Point out each leukocyte.
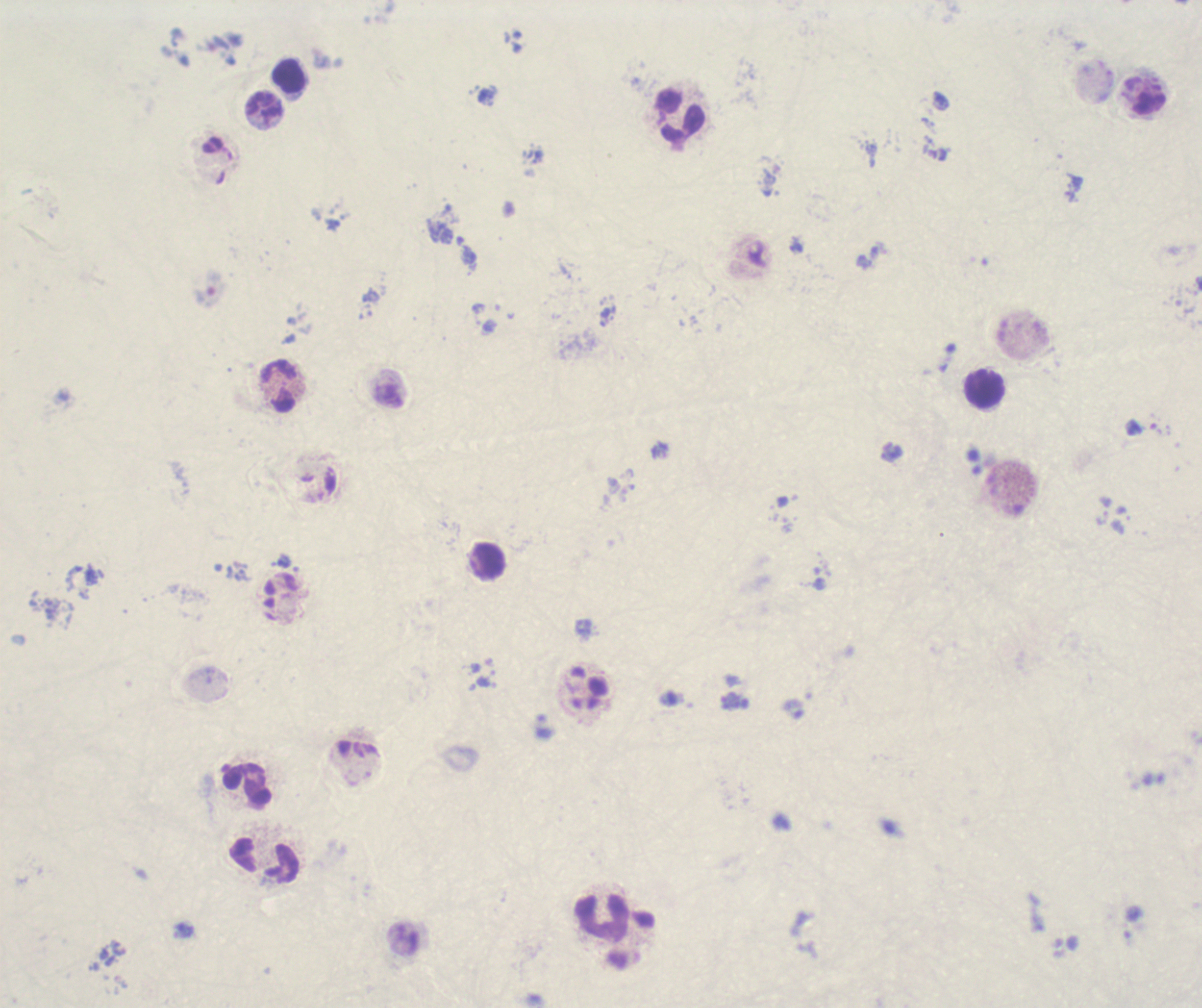

Approximate object centers, in pixels from the top-left corner.
Leukocytes: (x=289, y=75), (x=265, y=107), (x=681, y=115), (x=279, y=387), (x=985, y=390), (x=489, y=561), (x=247, y=784), (x=265, y=859), (x=601, y=918).

{
  "background_quality": "unsatisfactory",
  "stain": "Romanowsky",
  "field_of_view": "one from this slide",
  "context": "previously used in a real diagnosis",
  "magnification": "100x",
  "preparation": "thick smear of blood",
  "result": "Plasmodium parasites identified",
  "image_size": "1202×1008 pixels",
  "trophozoite_locations": "approximate object centers, in pixels from the top-left corner: (x=730, y=700)"
}